Point out each malaria parasite.
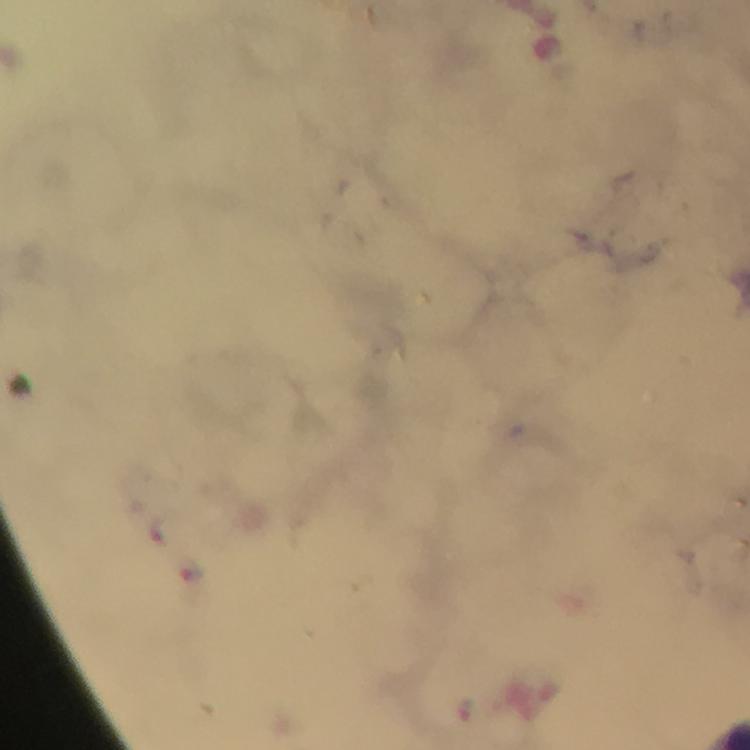
Approximate object centers, in pixels from the top-left corner.
Malaria parasites: (x=164, y=529), (x=192, y=573), (x=468, y=710).

Summary:
  - Preparation: thick blood film
  - Magnification: 100x
  - Cropped from: a single field of view
  - Immersion oil: used
  - Image size: 750×750 pixels
  - Stain: Giemsa
  - Context: from a diagnostic examination for malaria
  - Capture: smartphone mounted on the microscope